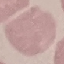

Summary:
  - Result: no malaria parasites seen
  - Preparation: thin smear
  - Image type: automatically extracted cell patch, resized to 64 × 64 pixels
  - Stain: Giemsa
  - Capture: smartphone camera at the microscope eyepiece